Locate every blood parasite and identify its species.
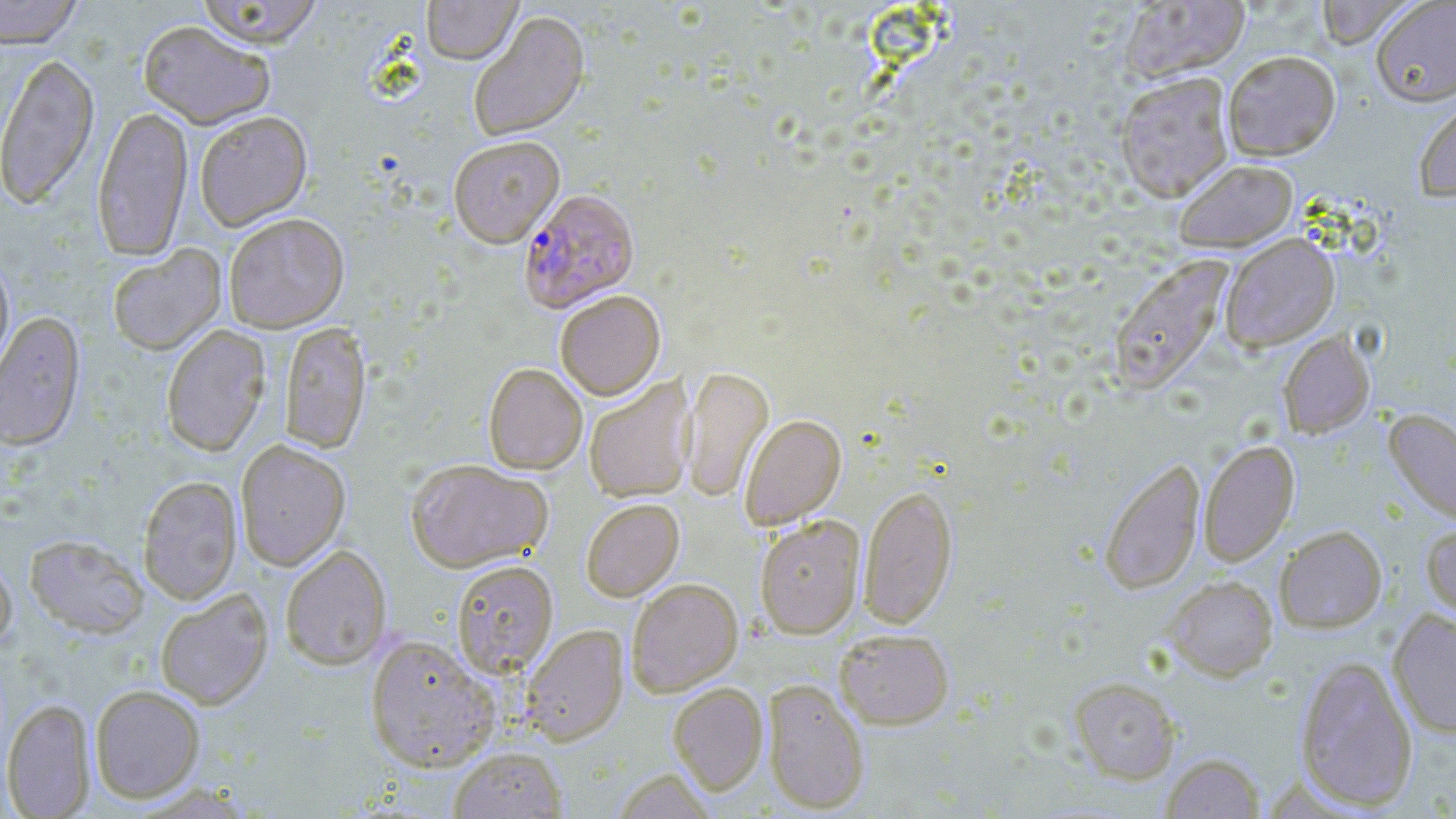
Approximate bounding boxes as named x1/y1/x2/y2 corners in pixels.
Plasmodium falciparum-infected red blood cells: (x1=518, y1=189, x2=640, y2=313).
No Plasmodium ovale, Plasmodium malariae, Plasmodium vivax, Babesia divergens, or Trypanosoma brucei observed.

Uninfected red blood cell locations: (x1=0, y1=0, x2=84, y2=48), (x1=194, y1=0, x2=325, y2=49), (x1=421, y1=0, x2=523, y2=67), (x1=1312, y1=0, x2=1417, y2=49), (x1=1371, y1=0, x2=1456, y2=106), (x1=1117, y1=1, x2=1250, y2=82), (x1=469, y1=12, x2=590, y2=144), (x1=138, y1=21, x2=275, y2=130), (x1=1222, y1=50, x2=1340, y2=160), (x1=0, y1=51, x2=99, y2=210), (x1=1115, y1=71, x2=1236, y2=202), (x1=1413, y1=95, x2=1456, y2=201), (x1=91, y1=106, x2=193, y2=261), (x1=195, y1=111, x2=312, y2=230), (x1=448, y1=137, x2=565, y2=248), (x1=1173, y1=159, x2=1297, y2=252), (x1=224, y1=213, x2=349, y2=332), (x1=1219, y1=233, x2=1340, y2=351), (x1=107, y1=244, x2=226, y2=355), (x1=0, y1=252, x2=14, y2=378), (x1=1108, y1=255, x2=1232, y2=394), (x1=555, y1=291, x2=665, y2=400), (x1=0, y1=310, x2=85, y2=450), (x1=279, y1=322, x2=372, y2=453), (x1=161, y1=324, x2=271, y2=456), (x1=1278, y1=331, x2=1375, y2=438), (x1=483, y1=363, x2=587, y2=475), (x1=680, y1=367, x2=773, y2=503), (x1=584, y1=377, x2=696, y2=503), (x1=1384, y1=408, x2=1456, y2=526), (x1=740, y1=414, x2=846, y2=530), (x1=236, y1=440, x2=350, y2=571), (x1=1199, y1=440, x2=1299, y2=566), (x1=1099, y1=457, x2=1205, y2=594), (x1=406, y1=459, x2=552, y2=572), (x1=138, y1=476, x2=242, y2=604), (x1=859, y1=483, x2=957, y2=630), (x1=581, y1=499, x2=684, y2=601), (x1=755, y1=516, x2=865, y2=638), (x1=1421, y1=521, x2=1456, y2=626), (x1=1274, y1=524, x2=1387, y2=633), (x1=25, y1=534, x2=148, y2=637), (x1=280, y1=545, x2=392, y2=670), (x1=0, y1=553, x2=16, y2=652), (x1=451, y1=560, x2=559, y2=677), (x1=1163, y1=576, x2=1278, y2=680), (x1=627, y1=579, x2=743, y2=696), (x1=155, y1=589, x2=273, y2=710), (x1=1388, y1=609, x2=1456, y2=738), (x1=521, y1=624, x2=628, y2=745), (x1=834, y1=629, x2=954, y2=729), (x1=365, y1=635, x2=500, y2=772), (x1=1295, y1=654, x2=1418, y2=811), (x1=1069, y1=677, x2=1181, y2=783), (x1=762, y1=678, x2=870, y2=813), (x1=668, y1=682, x2=768, y2=795), (x1=90, y1=684, x2=205, y2=802), (x1=2, y1=698, x2=95, y2=818), (x1=448, y1=745, x2=567, y2=818), (x1=1160, y1=753, x2=1265, y2=818). Slide-level diagnosis: Plasmodium falciparum. May-Grünwald-Giemsa-stained preparation. One field of a larger specimen. Image is 1456×819 pixels. Captured at 1000x magnification. Thin blood smear. Light microscopy.